State the preparation type.
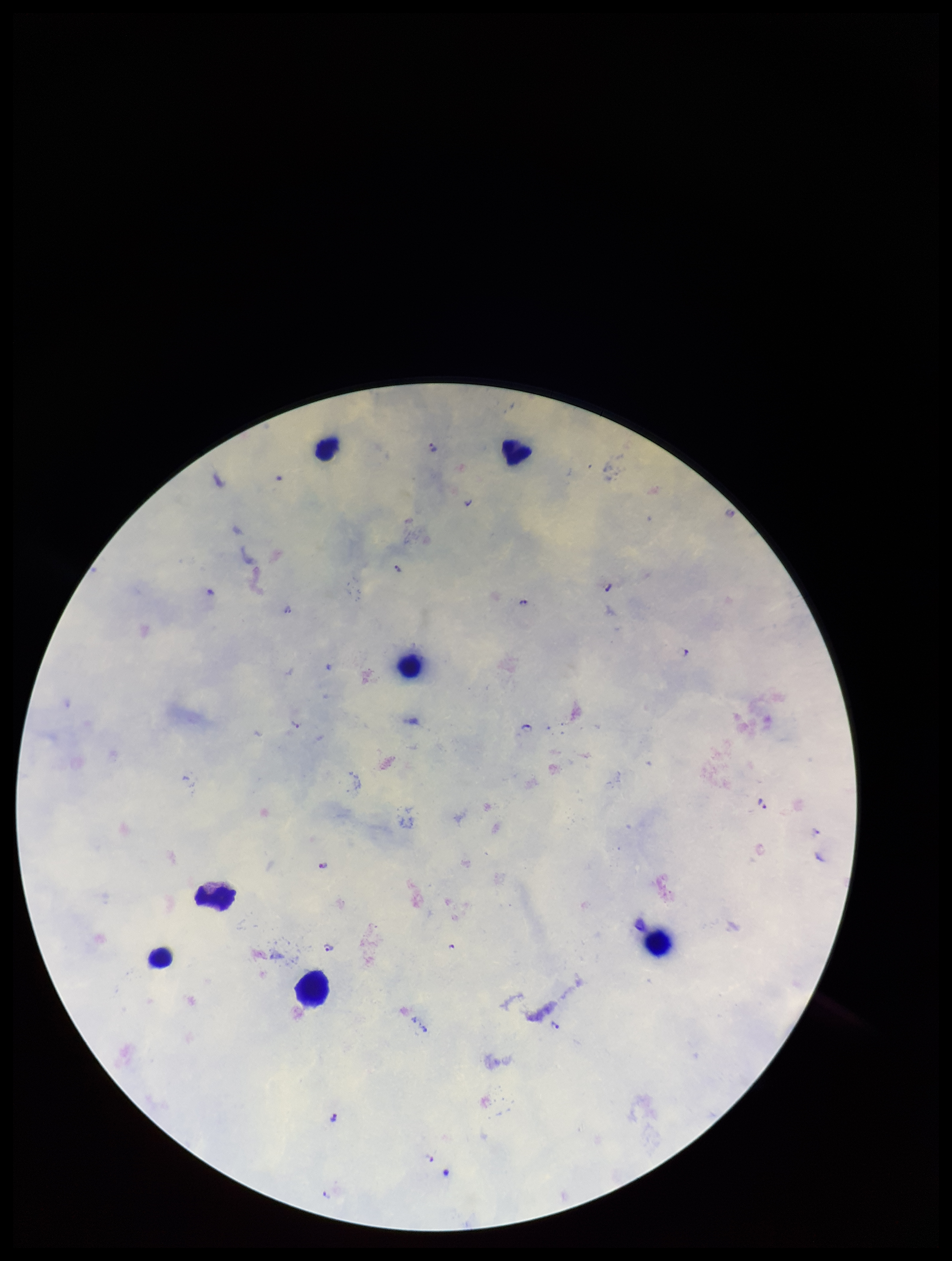

It is a thick blood smear.

Leukocyte count: 7. Parasite count: 14. Plasmodium parasites: detected. Species reported for this patient: Plasmodium falciparum. Patient malaria status: infected. Image is 952×1261 pixels. One field from this slide. Giemsa stain. Smartphone photograph taken through the eyepiece of a microscope.